Report the malaria status of this cell.
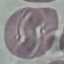
Uninfected.

Summary:
  - Capture: smartphone through the microscope eyepiece
  - Preparation: thin blood smear
  - Image type: cell patch, automatically extracted from a larger field of view and resized to 64 × 64 pixels
  - Stain: Giemsa